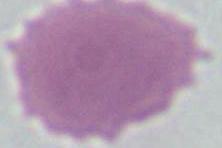

Micrograph. An erythrocyte is shown. Captured at 1000x magnification.